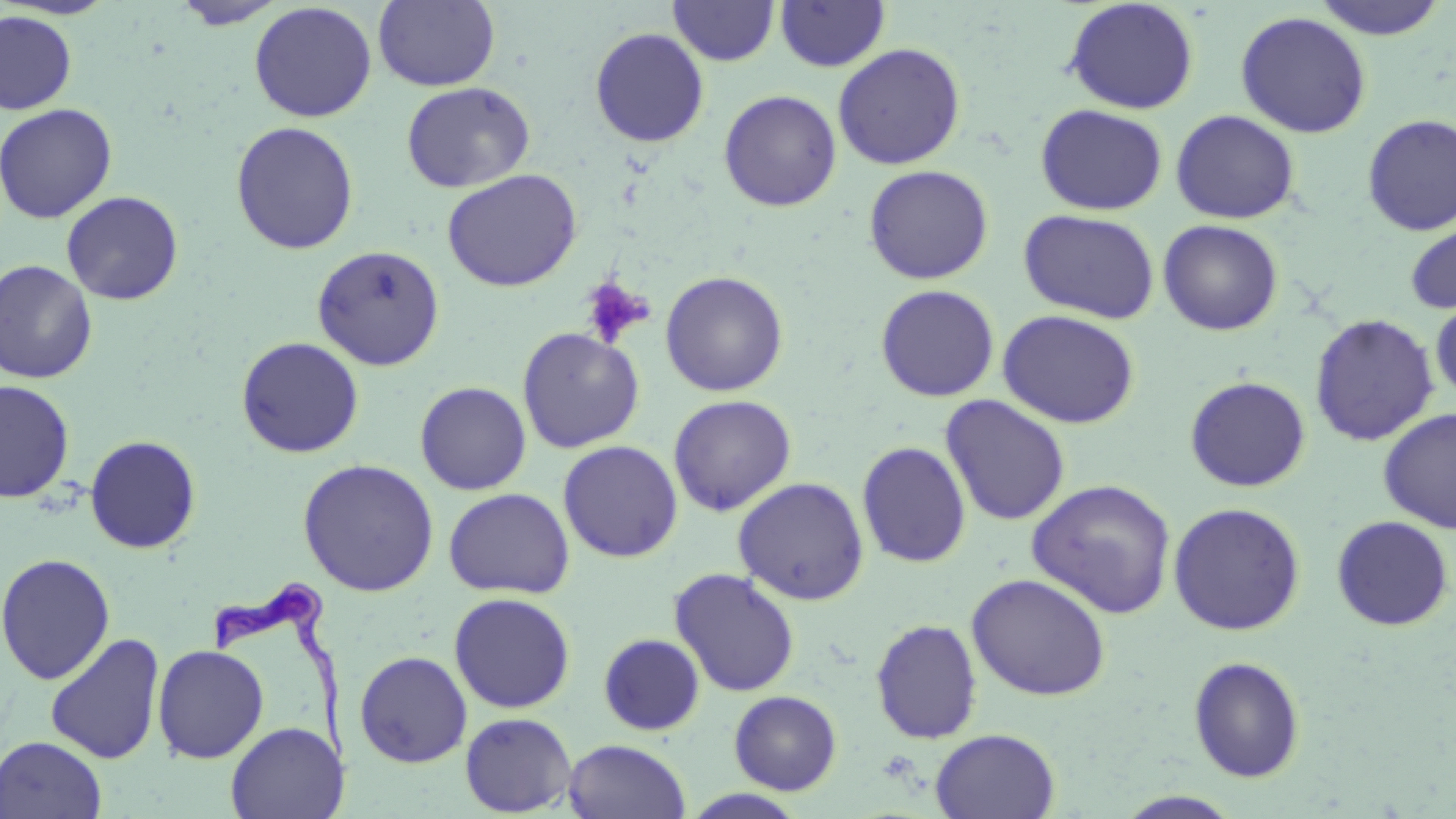

slide-level diagnosis = Trypanosoma brucei
platelet locations = approximate bounding boxes as [x1, y1, x2, y2] in pixels: [580, 276, 653, 347]
magnification = 1000x
Trypanosoma brucei locations = approximate bounding boxes as [x1, y1, x2, y2] in pixels: [205, 570, 361, 779]
stain = May-Grünwald-Giemsa
field of view = single
uninfected red blood cell locations = approximate bounding boxes as [x1, y1, x2, y2] in pixels: [1, 0, 120, 21], [373, 0, 501, 92], [669, 0, 780, 66], [774, 0, 891, 72], [1063, 0, 1199, 114], [1310, 0, 1450, 40], [172, 1, 287, 29], [249, 2, 377, 122], [0, 10, 77, 115], [1235, 10, 1372, 138], [590, 27, 710, 148], [832, 43, 966, 170], [401, 82, 535, 193], [719, 90, 842, 211], [0, 103, 117, 223], [1035, 104, 1168, 216], [1170, 109, 1300, 224], [1361, 114, 1456, 236], [230, 121, 359, 255], [863, 164, 994, 285], [442, 169, 582, 292], [61, 191, 184, 305], [1018, 209, 1159, 324], [1404, 216, 1456, 314], [1158, 219, 1283, 336], [312, 244, 445, 371], [0, 259, 99, 384], [659, 270, 789, 396], [875, 284, 999, 402], [1430, 296, 1456, 403], [999, 309, 1139, 428], [1309, 313, 1439, 447], [517, 327, 645, 453], [236, 336, 364, 458], [1185, 376, 1311, 492], [1, 379, 74, 503], [414, 381, 531, 495], [668, 394, 796, 516], [939, 395, 1071, 526], [1378, 407, 1456, 533], [85, 435, 201, 553], [558, 440, 683, 563], [856, 441, 971, 568], [298, 459, 439, 597], [732, 477, 870, 605], [1027, 479, 1178, 619], [443, 488, 574, 599], [1167, 502, 1306, 636], [1331, 515, 1454, 631], [1, 553, 116, 684], [668, 567, 801, 697], [966, 573, 1112, 701], [448, 592, 576, 714], [870, 619, 983, 744], [44, 633, 165, 764], [598, 633, 705, 736], [152, 644, 269, 763], [354, 650, 472, 768], [1188, 656, 1306, 783], [728, 690, 842, 795], [459, 712, 577, 817], [225, 722, 345, 819], [930, 728, 1060, 818], [0, 736, 107, 819], [563, 739, 691, 819], [680, 789, 810, 819], [1114, 791, 1245, 818]
preparation = thin blood film
modality = light microscopy
image size = 1456×819 pixels